Name the parasite shown.
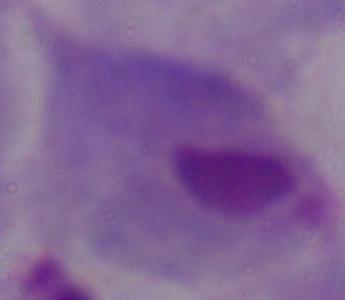
This is a trichomonad.

modality = micrograph
magnification = 1000x